Assess the morphology of the red blood cells.
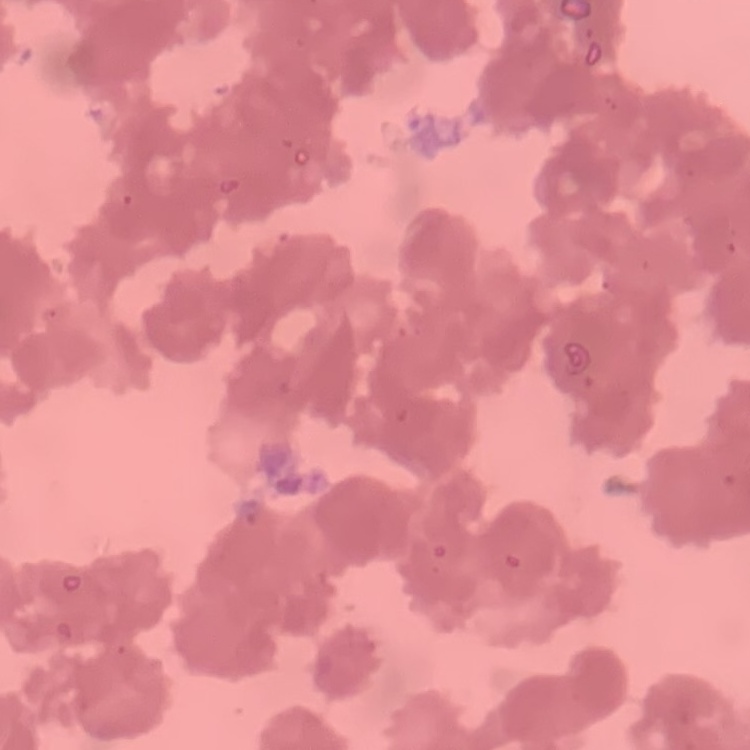

Rouleaux formation.

Square crop of a larger photomicrograph. Thin blood smear. Stained with either Field's or Giemsa.